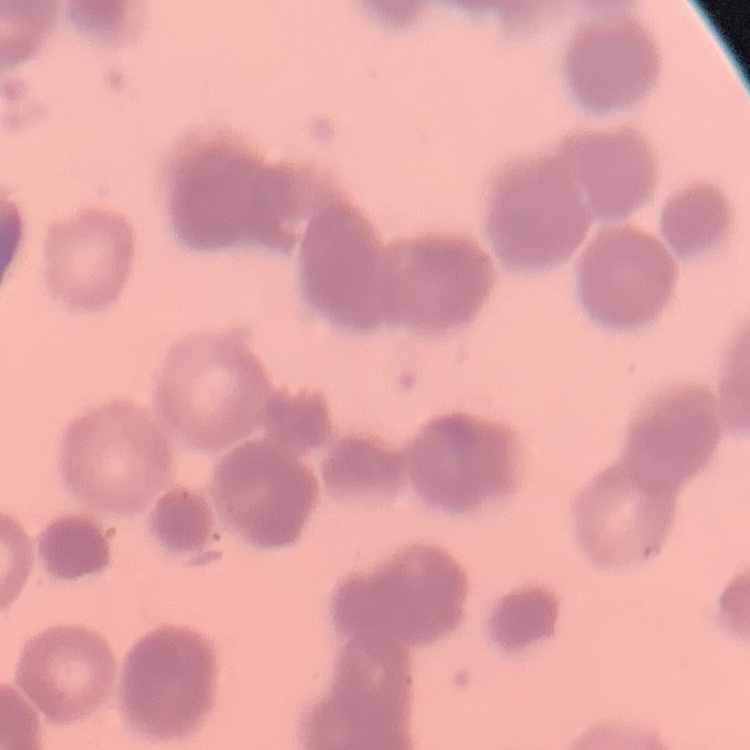

Summary:
  - Erythrocyte morphology: rouleaux formation
  - Preparation: thin peripheral smear
  - Stain: Field's or Giemsa
  - Image type: square crop of a larger photomicrograph